Classify this cell by malaria status.
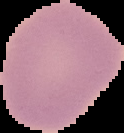
Uninfected.

Summary:
  - Image size: 124×133 pixels
  - Image type: segmented cell region on a black background
  - Preparation: thin blood film